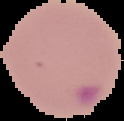 From a thin blood smear. Result: malaria parasites identified. Image is 124×121 pixels. The area outside the segmented cell region is set to black.